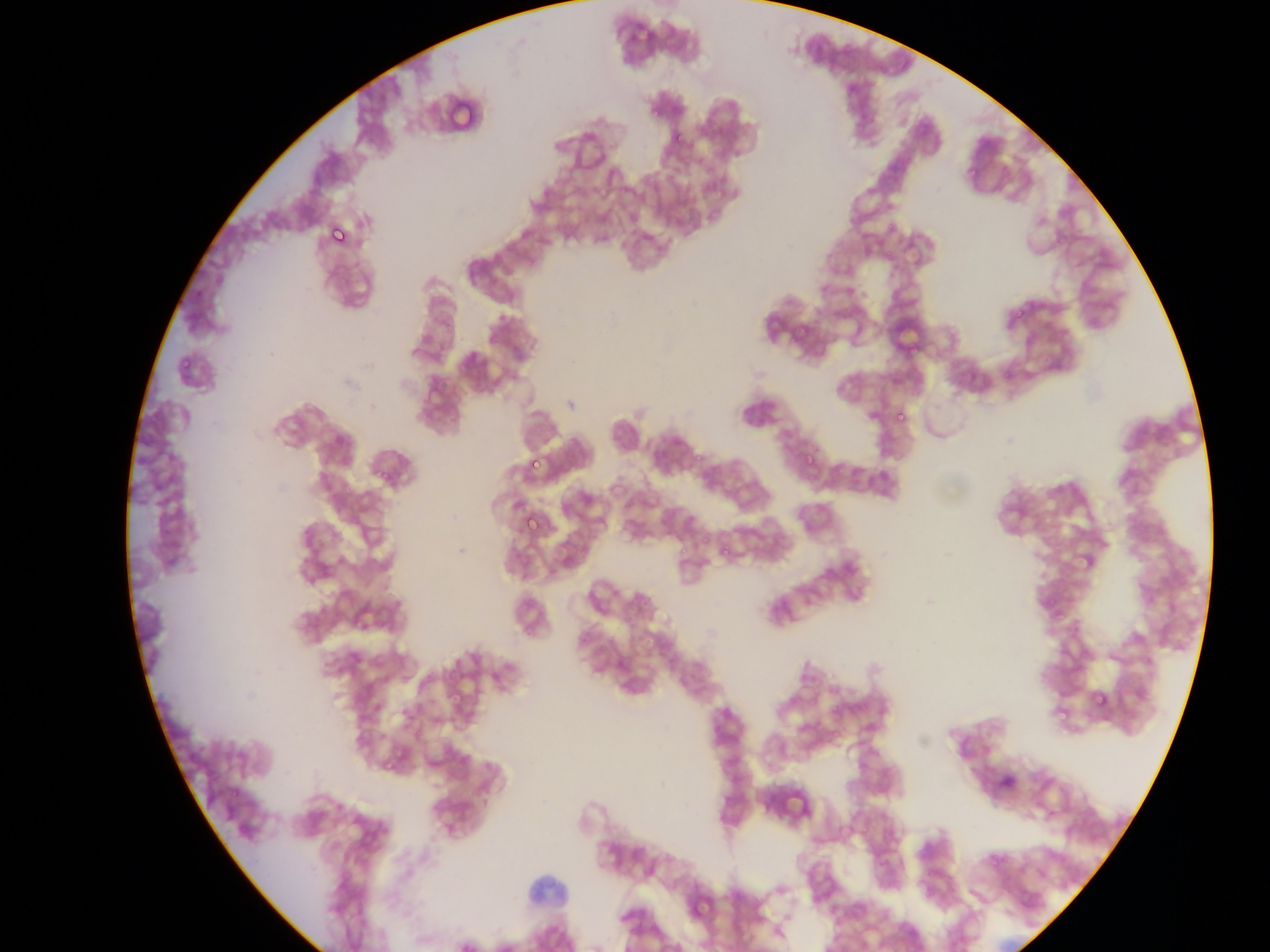
leukocyte locations = approximate bounding boxes as [left, top, right, bottom] in pixels: [521, 866, 577, 914]
malaria parasite locations = approximate bounding boxes as [left, top, right, bottom] in pixels: [672, 133, 683, 145], [967, 166, 978, 177], [325, 221, 349, 245], [1011, 307, 1026, 322], [895, 409, 907, 422], [800, 453, 820, 473], [526, 455, 541, 471], [368, 463, 393, 487], [522, 514, 536, 529], [699, 534, 711, 545], [719, 545, 730, 556], [1045, 597, 1060, 610], [300, 612, 315, 625], [450, 689, 462, 707], [1092, 691, 1110, 709], [1055, 714, 1068, 731], [379, 754, 401, 778], [229, 787, 241, 801]
field of view = single
country = Ghana
capture = mobile-phone photograph through a microscope
image size = 1270×952 pixels
preparation = thin blood smear